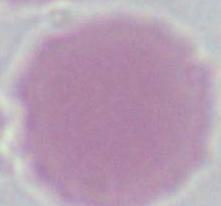

modality = photomicrograph
identification = red blood cell
magnification = 1000x